Give the preparation type.
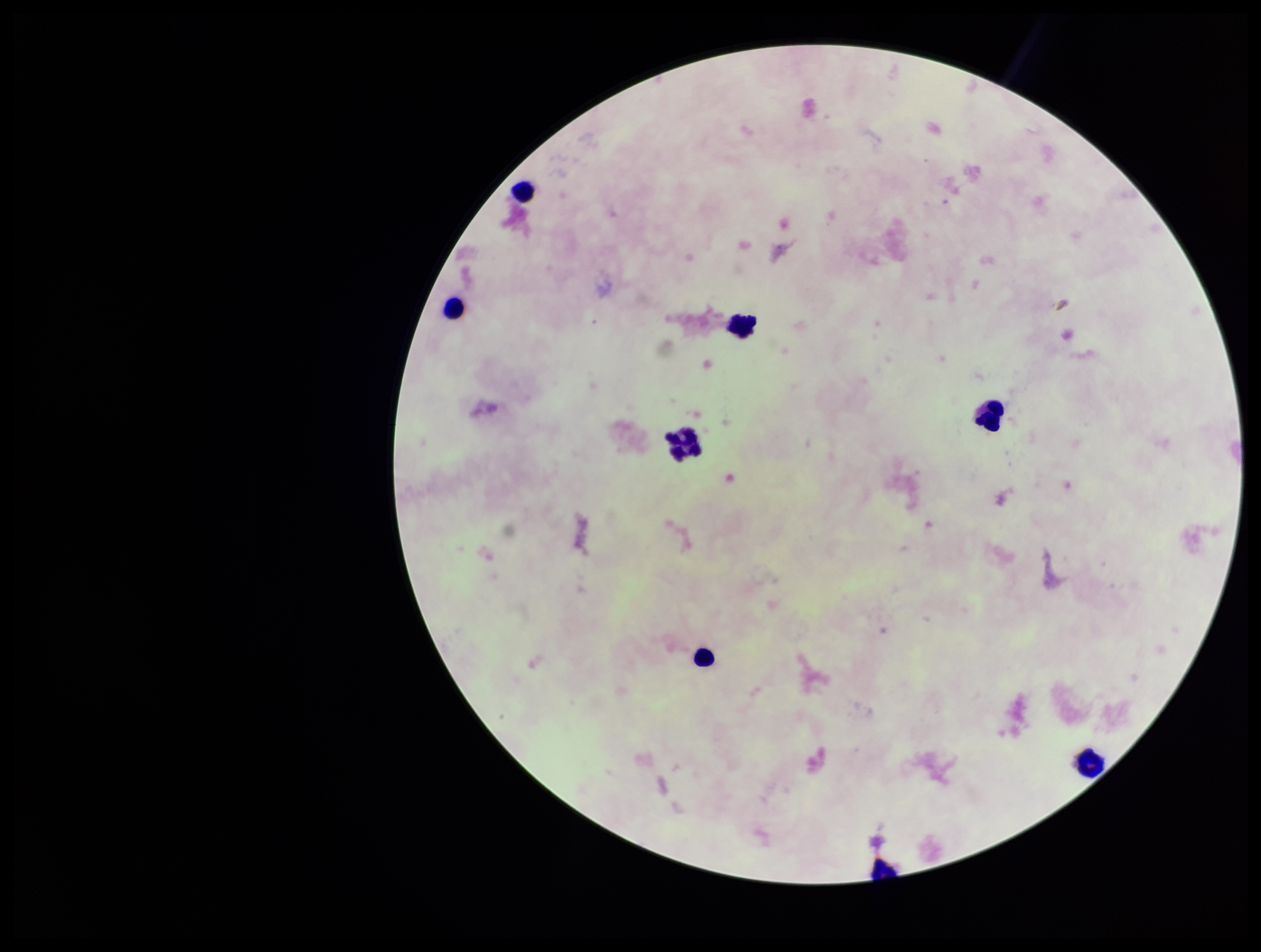
It is a thick blood smear.

Summary:
  - Image size: 1261×952 pixels
  - Field of view: single
  - Capture: smartphone photograph through the microscope eyepiece
  - Parasite count: 0
  - Patient malaria status: negative
  - Stain: Giemsa
  - Plasmodium parasites: none seen
  - Leukocyte count: 8